Classify this cell by malaria status.
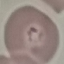

It is parasitized.

{
  "capture": "smartphone camera at the microscope eyepiece",
  "preparation": "thin blood smear",
  "image_type": "automatically extracted cell patch, resized to 64 × 64 pixels",
  "stain": "Giemsa"
}